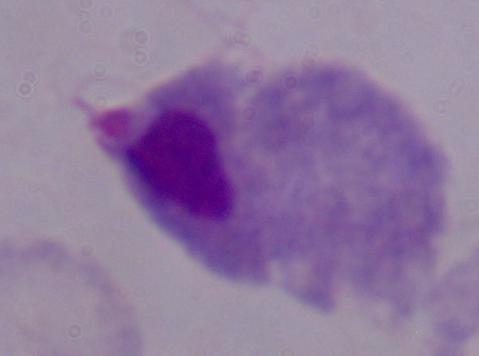

A trichomonad is shown. 1000x magnification. Photomicrograph.